State which parasite is depicted.
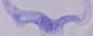
This is a trypanosome.

Photomicrograph. 1000x magnification.